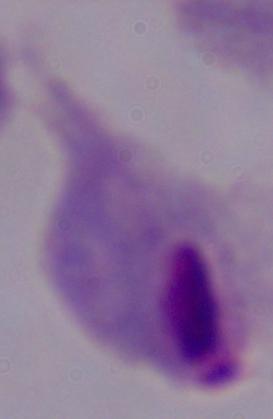
Summary:
  - Magnification: 1000x
  - Identification: trichomonad
  - Modality: micrograph